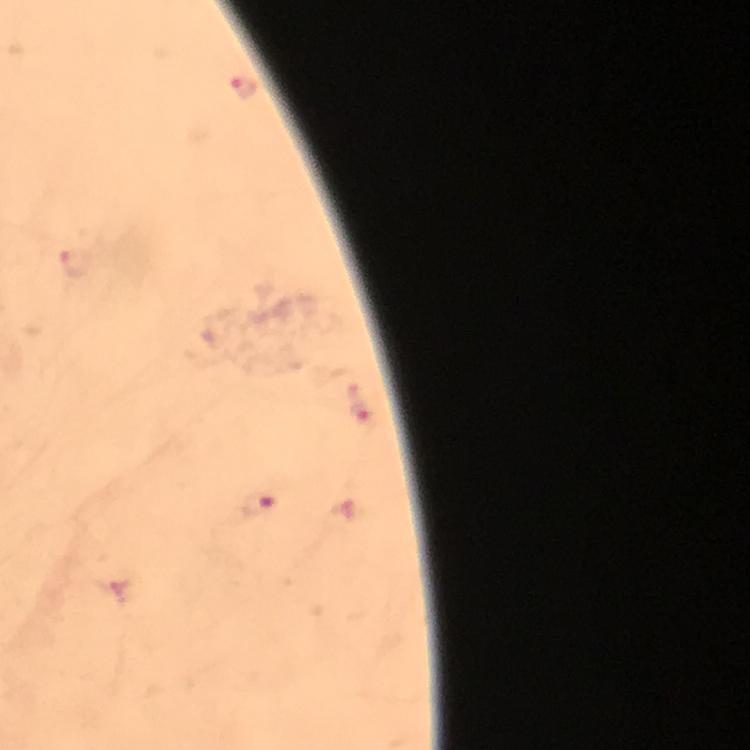
Approximate centers as [x, y] in pixels.
Summary:
  - Plasmodium parasite locations: [243, 86], [76, 264], [362, 401], [258, 504]
  - Magnification: 100x
  - Image size: 750×750 pixels
  - Immersion oil: applied
  - Capture: smartphone camera through the microscope
  - Context: from a diagnostic examination for malaria
  - Stain: Giemsa
  - Cropped from: a single field of view
  - Preparation: thick blood smear